Identify the blood parasite species.
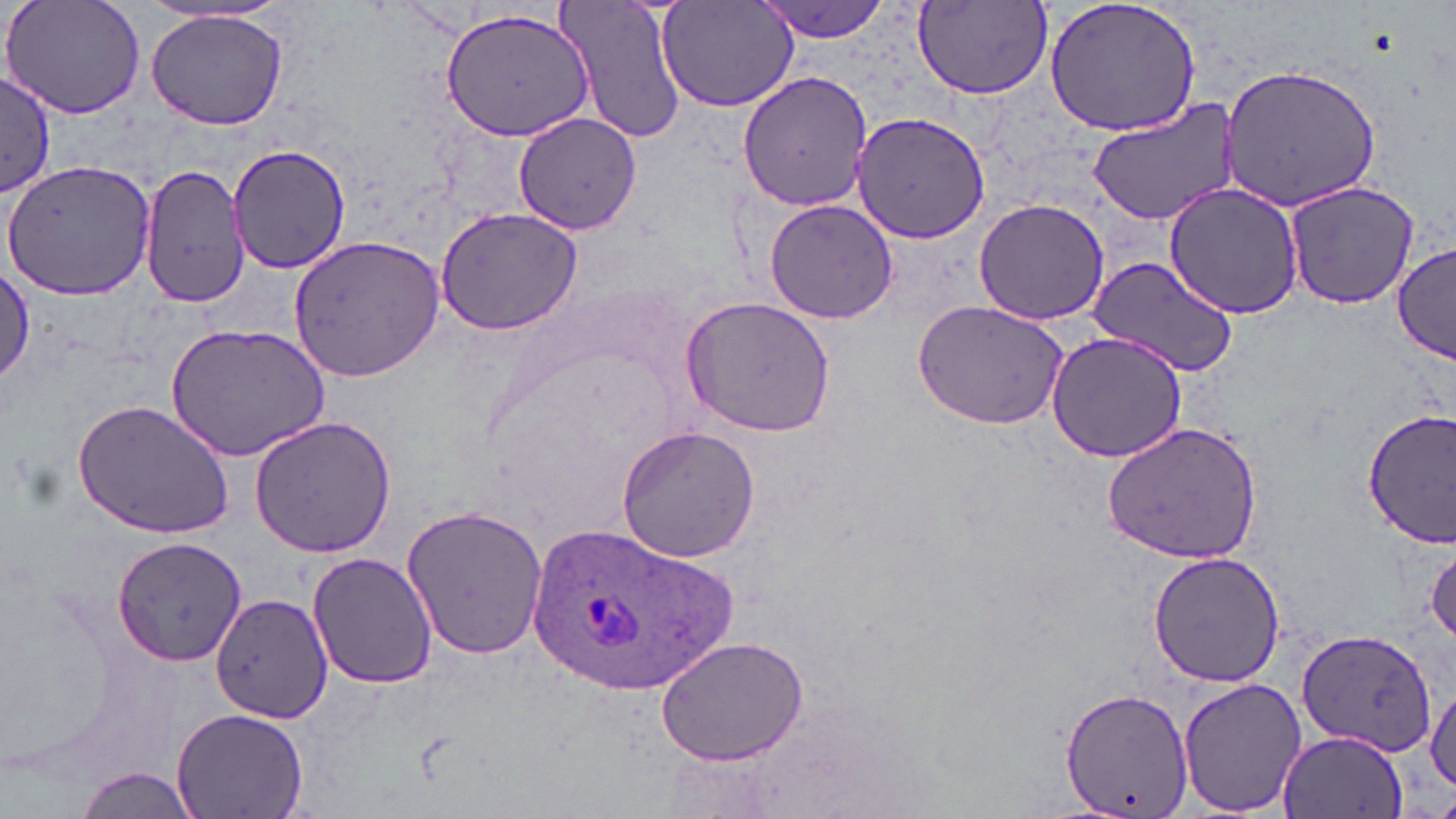

Plasmodium ovale.

magnification = 1000x
Plasmodium ovale-infected red blood cell locations = approximate bounding boxes as (x1, y1, x2, y2) in pixels: (521, 517, 735, 697)
image size = 1456×819 pixels
modality = optical microscopy
stain = May-Grünwald-Giemsa
field of view = single
uninfected red blood cell locations = approximate bounding boxes as (x1, y1, x2, y2) in pixels: (558, 0, 689, 145), (752, 0, 892, 41), (1044, 0, 1203, 139), (4, 1, 148, 121), (656, 2, 799, 114), (912, 2, 1054, 101), (439, 7, 594, 140), (145, 10, 291, 131), (1219, 63, 1383, 213), (737, 69, 876, 212), (0, 71, 58, 196), (1085, 101, 1242, 226), (512, 112, 642, 235), (850, 112, 992, 245), (227, 145, 354, 275), (2, 157, 159, 300), (138, 163, 251, 309), (1283, 179, 1423, 310), (1163, 181, 1304, 320), (762, 198, 898, 324), (974, 198, 1109, 325), (434, 206, 585, 337), (288, 234, 445, 383), (1393, 244, 1456, 365), (1087, 255, 1241, 378), (0, 267, 34, 389), (681, 295, 837, 438), (912, 299, 1070, 430), (164, 322, 332, 463), (1046, 330, 1189, 463), (72, 399, 235, 538), (1361, 408, 1456, 549), (248, 416, 396, 559), (615, 423, 763, 562), (1101, 423, 1262, 564), (401, 503, 553, 664), (114, 536, 247, 665), (1427, 544, 1456, 645), (1147, 550, 1286, 688), (306, 552, 439, 690), (210, 591, 333, 723), (1296, 627, 1437, 757), (655, 637, 810, 766), (1177, 676, 1309, 817), (1426, 683, 1456, 793), (1060, 687, 1192, 816), (172, 705, 308, 819), (1275, 728, 1410, 818), (74, 767, 195, 819)
preparation = thin blood film